Name the parasite shown.
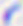
Toxoplasma gondii.

modality: photomicrograph
magnification: 400x